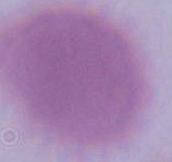

A red blood cell is shown. Photomicrograph. Captured at 1000x magnification.